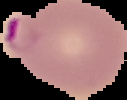

{
  "malaria_status": "parasitized",
  "image_size": "127×100 pixels",
  "image_type": "segmented cell region on a black background",
  "preparation": "thin blood film"
}